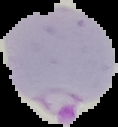 Cell region segmented out of the field of view; the surrounding area is masked to black. Image is 118×127 pixels. From a thin blood film. Result: malaria parasites detected.